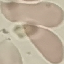

Result: no malaria parasites detected. Cell patch, automatically extracted from a larger field of view and resized to 64 × 64 pixels. Giemsa-stained preparation. Acquired by smartphone through the microscope eyepiece. Thin blood smear.